Assess the morphology of the red blood cells.
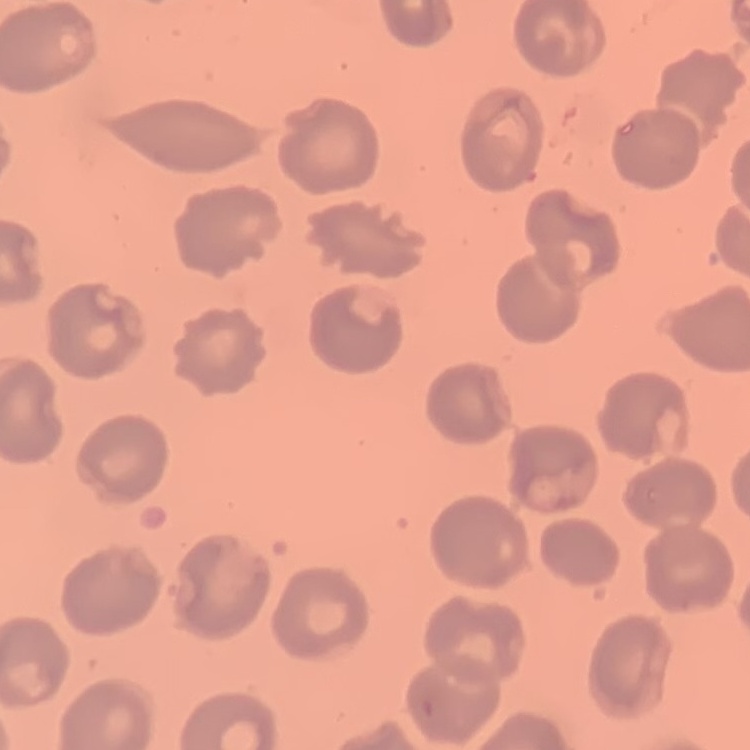
They show no rouleaux formation.

Summary:
  - Image type: square crop of a larger photomicrograph
  - Preparation: thin blood smear
  - Stain: Field's or Giemsa